Report the malaria status of this cell.
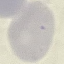
Uninfected.

Giemsa-stained preparation. Thin blood film. Acquired by smartphone through the microscope eyepiece. Automatically extracted cell patch, resized to 64 × 64 pixels.